Evaluate for Plasmodium parasites.
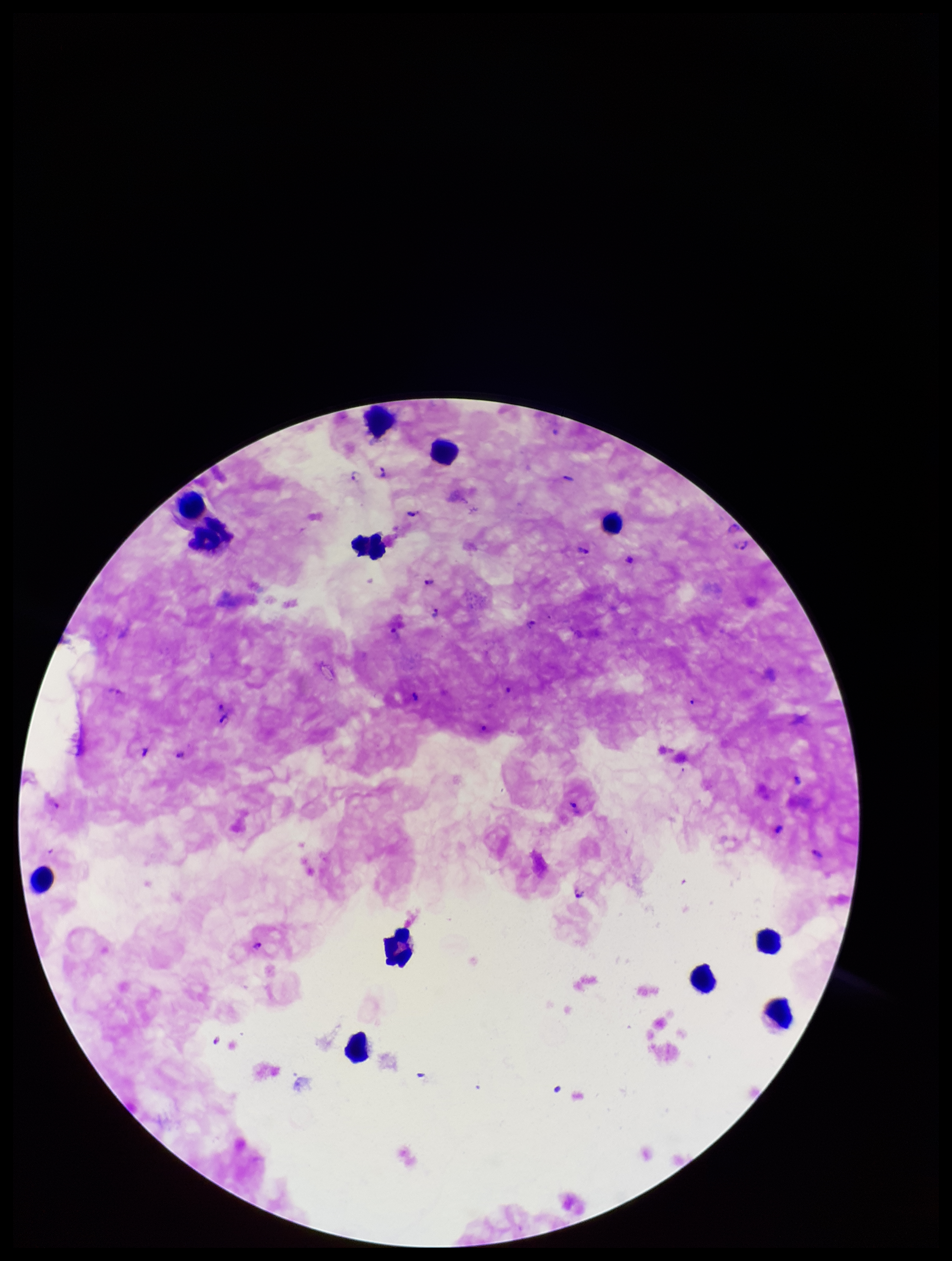
Identified.

Photographed through the microscope eyepiece with a smartphone camera. Image is 952×1261 pixels. Leukocyte count: 12. Parasite count: 23. Patient malaria status: infected. Stained with Giemsa. Species reported for this patient: Plasmodium falciparum. One field from this slide. Preparation: thick smear.